Name the blood parasite species.
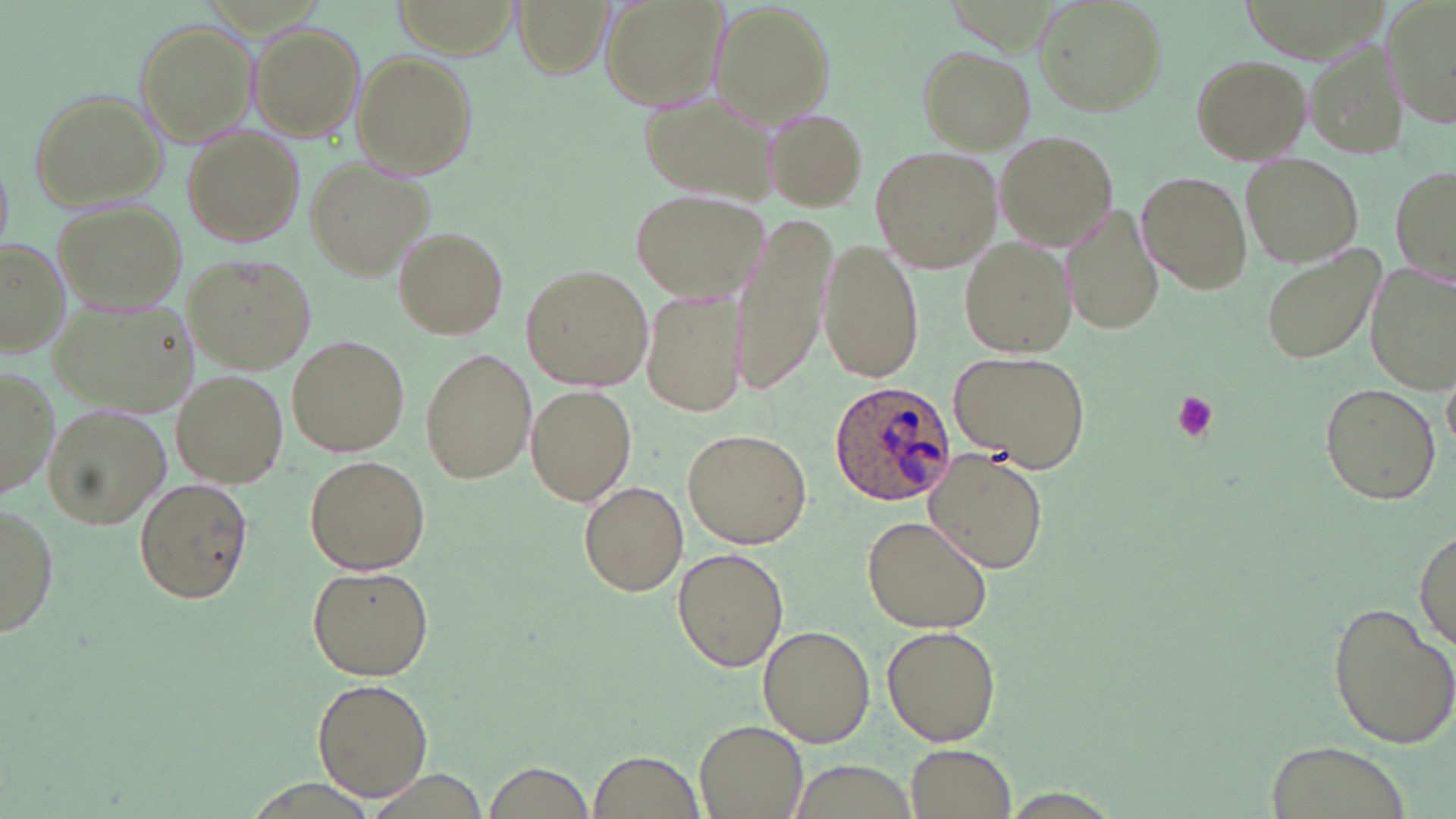

Plasmodium ovale.

magnification = 1000x
preparation = thin blood smear
Plasmodium ovale-infected red blood cell locations = approximate bounding boxes as named x1/y1/x2/y2 corners in pixels: (x1=829, y1=378, x2=960, y2=504)
image size = 1456×819 pixels
stain = May-Grünwald-Giemsa
field of view = one of a larger specimen
platelet locations = approximate bounding boxes as named x1/y1/x2/y2 corners in pixels: (x1=1169, y1=391, x2=1220, y2=442)
uninfected red blood cell locations = approximate bounding boxes as named x1/y1/x2/y2 corners in pixels: (x1=512, y1=0, x2=613, y2=78), (x1=601, y1=0, x2=727, y2=112), (x1=1034, y1=0, x2=1164, y2=114), (x1=1383, y1=0, x2=1456, y2=131), (x1=711, y1=3, x2=834, y2=126), (x1=135, y1=19, x2=257, y2=144), (x1=250, y1=21, x2=365, y2=140), (x1=1307, y1=40, x2=1403, y2=156), (x1=917, y1=45, x2=1035, y2=151), (x1=352, y1=51, x2=477, y2=178), (x1=1190, y1=52, x2=1312, y2=166), (x1=27, y1=90, x2=169, y2=211), (x1=638, y1=90, x2=779, y2=203), (x1=764, y1=109, x2=870, y2=211), (x1=182, y1=128, x2=303, y2=248), (x1=994, y1=132, x2=1119, y2=249), (x1=870, y1=147, x2=999, y2=272), (x1=304, y1=156, x2=434, y2=281), (x1=1241, y1=156, x2=1361, y2=269), (x1=1391, y1=164, x2=1455, y2=284), (x1=1136, y1=169, x2=1252, y2=295), (x1=630, y1=188, x2=770, y2=302), (x1=55, y1=202, x2=188, y2=313), (x1=1064, y1=206, x2=1164, y2=339), (x1=730, y1=207, x2=836, y2=395), (x1=395, y1=227, x2=508, y2=338), (x1=958, y1=234, x2=1075, y2=357), (x1=820, y1=236, x2=922, y2=382), (x1=0, y1=239, x2=71, y2=356), (x1=1260, y1=247, x2=1382, y2=367), (x1=183, y1=253, x2=315, y2=374), (x1=1367, y1=262, x2=1455, y2=389), (x1=521, y1=264, x2=653, y2=391), (x1=642, y1=289, x2=748, y2=417), (x1=49, y1=294, x2=197, y2=421), (x1=287, y1=335, x2=409, y2=457), (x1=420, y1=347, x2=537, y2=483), (x1=947, y1=350, x2=1095, y2=473), (x1=1, y1=369, x2=57, y2=503), (x1=1444, y1=371, x2=1455, y2=454), (x1=173, y1=372, x2=287, y2=487), (x1=1318, y1=382, x2=1441, y2=505), (x1=525, y1=385, x2=640, y2=508), (x1=43, y1=404, x2=171, y2=530), (x1=684, y1=427, x2=812, y2=548), (x1=924, y1=450, x2=1048, y2=573), (x1=303, y1=454, x2=431, y2=576), (x1=133, y1=479, x2=253, y2=605), (x1=579, y1=481, x2=687, y2=598), (x1=0, y1=500, x2=57, y2=639), (x1=862, y1=515, x2=993, y2=633), (x1=1415, y1=531, x2=1455, y2=648), (x1=673, y1=547, x2=790, y2=673), (x1=306, y1=565, x2=434, y2=681), (x1=1325, y1=599, x2=1456, y2=749), (x1=759, y1=625, x2=875, y2=748), (x1=882, y1=625, x2=1001, y2=747), (x1=313, y1=677, x2=435, y2=804), (x1=695, y1=719, x2=809, y2=819), (x1=1267, y1=739, x2=1405, y2=819), (x1=903, y1=744, x2=1018, y2=818), (x1=589, y1=750, x2=703, y2=818), (x1=787, y1=761, x2=921, y2=816), (x1=484, y1=762, x2=596, y2=816), (x1=995, y1=788, x2=1127, y2=819)
modality = optical microscopy